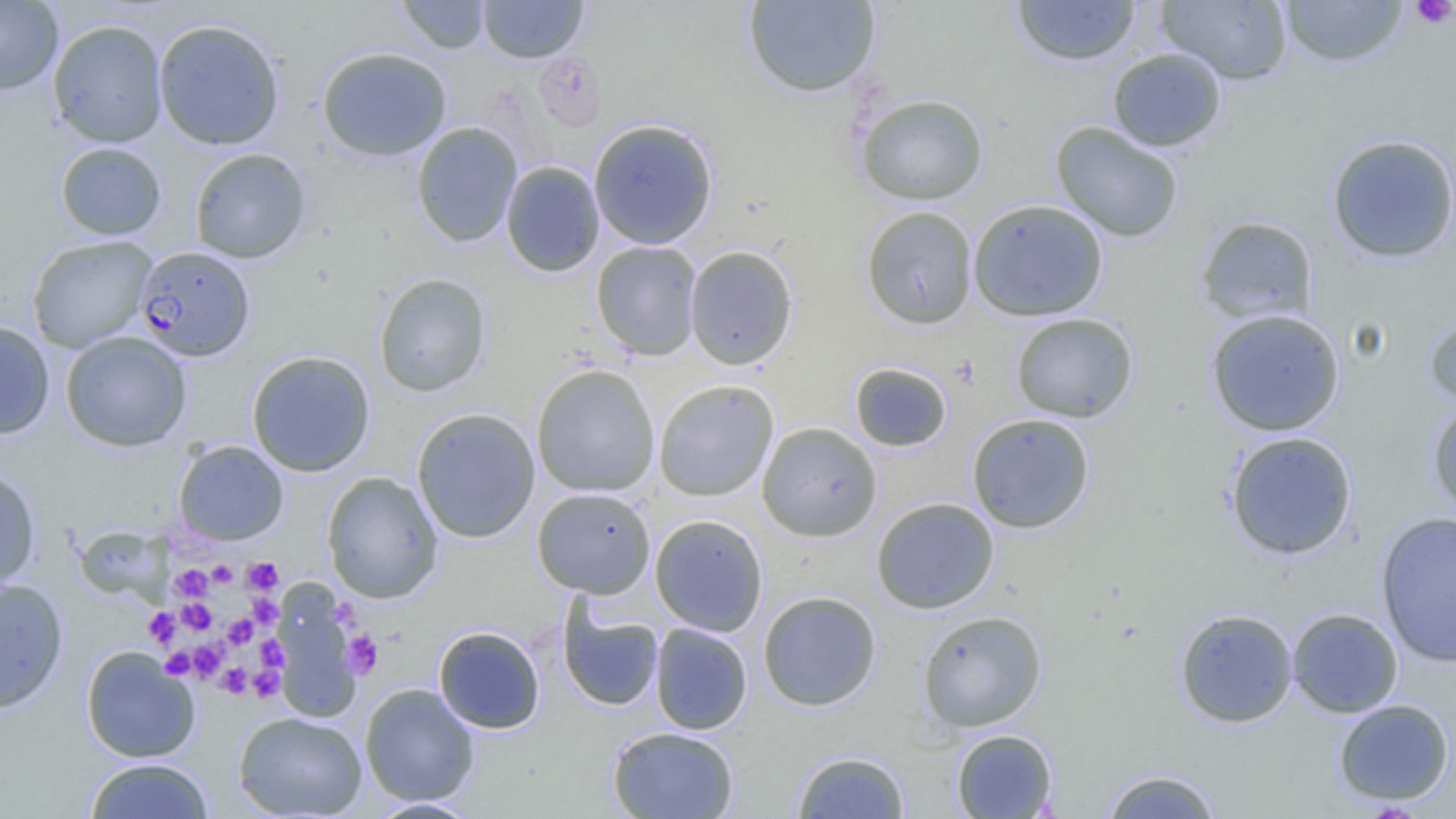
Approximate bounding boxes as named x1/y1/x2/y2 corners in pixels. Plasmodium falciparum-infected red blood cell locations: (x1=134, y1=246, x2=255, y2=362). Uninfected red blood cell locations: (x1=0, y1=0, x2=63, y2=95), (x1=396, y1=0, x2=490, y2=54), (x1=743, y1=0, x2=882, y2=98), (x1=1156, y1=0, x2=1294, y2=85), (x1=1278, y1=0, x2=1409, y2=69), (x1=478, y1=1, x2=588, y2=63), (x1=1012, y1=1, x2=1141, y2=67), (x1=153, y1=18, x2=285, y2=150), (x1=48, y1=19, x2=168, y2=148), (x1=178, y1=20, x2=299, y2=259), (x1=316, y1=46, x2=452, y2=161), (x1=1107, y1=48, x2=1227, y2=152), (x1=533, y1=52, x2=607, y2=132), (x1=855, y1=92, x2=990, y2=206), (x1=588, y1=118, x2=719, y2=250), (x1=1049, y1=121, x2=1185, y2=242), (x1=411, y1=122, x2=523, y2=248), (x1=1326, y1=134, x2=1456, y2=264), (x1=55, y1=142, x2=167, y2=241), (x1=189, y1=147, x2=311, y2=264), (x1=501, y1=161, x2=604, y2=277), (x1=968, y1=199, x2=1108, y2=322), (x1=860, y1=206, x2=978, y2=330), (x1=1195, y1=215, x2=1319, y2=325), (x1=26, y1=235, x2=156, y2=353), (x1=590, y1=241, x2=703, y2=361), (x1=684, y1=245, x2=798, y2=370), (x1=374, y1=272, x2=492, y2=397), (x1=1206, y1=308, x2=1345, y2=436), (x1=1010, y1=312, x2=1138, y2=424), (x1=1423, y1=312, x2=1456, y2=409), (x1=0, y1=320, x2=55, y2=440), (x1=60, y1=331, x2=192, y2=452), (x1=246, y1=350, x2=375, y2=477), (x1=849, y1=362, x2=953, y2=452), (x1=531, y1=364, x2=660, y2=497), (x1=653, y1=379, x2=779, y2=501), (x1=1426, y1=401, x2=1456, y2=519), (x1=412, y1=408, x2=540, y2=543), (x1=966, y1=413, x2=1096, y2=534), (x1=757, y1=422, x2=882, y2=542), (x1=1224, y1=431, x2=1358, y2=560), (x1=174, y1=440, x2=289, y2=545), (x1=0, y1=463, x2=41, y2=592), (x1=321, y1=471, x2=443, y2=603), (x1=532, y1=487, x2=656, y2=599), (x1=871, y1=497, x2=1000, y2=614), (x1=1375, y1=511, x2=1456, y2=667), (x1=650, y1=514, x2=768, y2=636), (x1=76, y1=524, x2=169, y2=607), (x1=0, y1=577, x2=68, y2=714), (x1=273, y1=579, x2=360, y2=721), (x1=757, y1=590, x2=882, y2=711), (x1=557, y1=600, x2=664, y2=712), (x1=1287, y1=607, x2=1403, y2=718), (x1=1175, y1=608, x2=1299, y2=728), (x1=917, y1=610, x2=1047, y2=732), (x1=650, y1=623, x2=753, y2=735), (x1=433, y1=625, x2=545, y2=734), (x1=81, y1=646, x2=199, y2=762), (x1=359, y1=683, x2=480, y2=806), (x1=1333, y1=698, x2=1455, y2=805), (x1=233, y1=711, x2=368, y2=818), (x1=607, y1=726, x2=740, y2=818), (x1=951, y1=729, x2=1058, y2=818), (x1=791, y1=751, x2=910, y2=818), (x1=83, y1=757, x2=215, y2=818), (x1=1098, y1=768, x2=1224, y2=818), (x1=366, y1=798, x2=482, y2=818). Platelet locations: (x1=1411, y1=0, x2=1455, y2=29), (x1=243, y1=557, x2=283, y2=595), (x1=207, y1=560, x2=237, y2=588), (x1=170, y1=564, x2=212, y2=602), (x1=249, y1=595, x2=281, y2=629), (x1=178, y1=598, x2=217, y2=635), (x1=330, y1=599, x2=361, y2=630), (x1=144, y1=607, x2=179, y2=647), (x1=223, y1=613, x2=257, y2=649), (x1=341, y1=630, x2=383, y2=678), (x1=254, y1=635, x2=288, y2=673), (x1=190, y1=638, x2=226, y2=681), (x1=160, y1=647, x2=197, y2=679), (x1=217, y1=663, x2=250, y2=697), (x1=249, y1=665, x2=285, y2=702). Slide-level diagnosis: Plasmodium falciparum. Thin blood film. Single field of view. 1000x magnification. Image is 1456×819 pixels. Optical microscopy.